Report the malaria status of this cell.
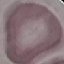

Uninfected.

Cell patch, automatically extracted from a larger field of view and resized to 64 × 64 pixels. Thin blood smear. Acquired by smartphone through the microscope eyepiece. Giemsa stain.